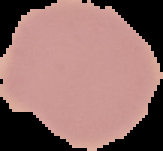
{
  "image_size": "163×151 pixels",
  "image_type": "segmented cell region on a black background",
  "preparation": "thin blood smear",
  "result": "no malaria parasites detected"
}